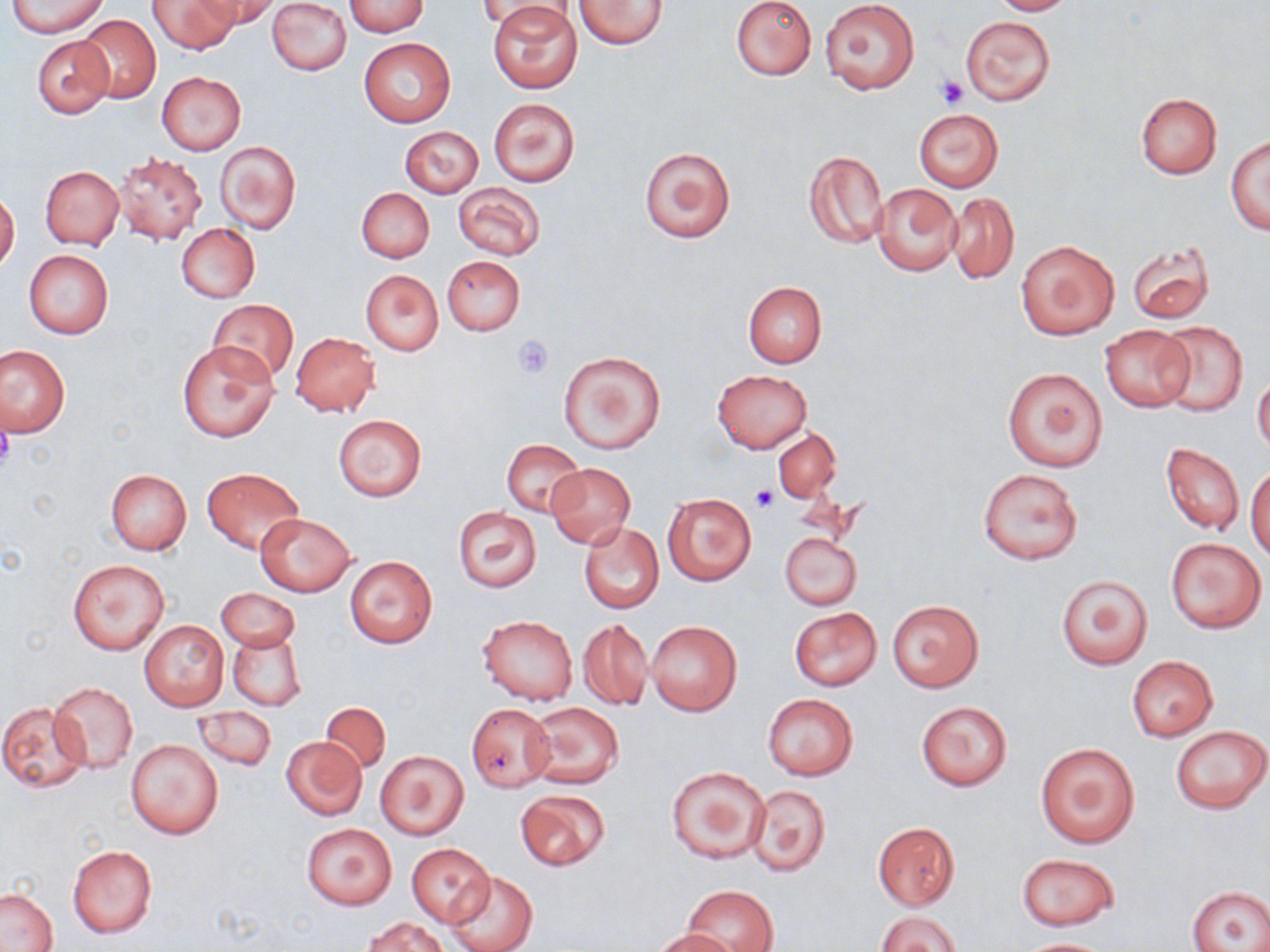

Approximate bounding boxes as named x1/y1/x2/y2 corners in pixels. Uninfected red blood cell locations: (x1=7, y1=0, x2=109, y2=38), (x1=148, y1=0, x2=237, y2=54), (x1=195, y1=0, x2=281, y2=34), (x1=267, y1=0, x2=352, y2=75), (x1=480, y1=0, x2=580, y2=28), (x1=731, y1=0, x2=817, y2=82), (x1=820, y1=0, x2=920, y2=93), (x1=991, y1=0, x2=1074, y2=15), (x1=343, y1=1, x2=429, y2=36), (x1=489, y1=1, x2=582, y2=94), (x1=574, y1=1, x2=668, y2=49), (x1=74, y1=14, x2=161, y2=103), (x1=961, y1=15, x2=1055, y2=106), (x1=33, y1=35, x2=115, y2=118), (x1=359, y1=38, x2=456, y2=128), (x1=157, y1=72, x2=247, y2=155), (x1=1134, y1=92, x2=1223, y2=180), (x1=489, y1=98, x2=579, y2=186), (x1=912, y1=108, x2=1004, y2=192), (x1=401, y1=126, x2=483, y2=197), (x1=1226, y1=136, x2=1270, y2=234), (x1=217, y1=142, x2=300, y2=234), (x1=638, y1=146, x2=736, y2=242), (x1=802, y1=148, x2=890, y2=250), (x1=113, y1=150, x2=206, y2=244), (x1=41, y1=165, x2=123, y2=249), (x1=871, y1=182, x2=962, y2=277), (x1=453, y1=183, x2=545, y2=259), (x1=356, y1=187, x2=434, y2=263), (x1=947, y1=192, x2=1019, y2=285), (x1=0, y1=193, x2=19, y2=271), (x1=177, y1=225, x2=259, y2=302), (x1=1016, y1=239, x2=1120, y2=340), (x1=1128, y1=244, x2=1214, y2=325), (x1=23, y1=249, x2=113, y2=339), (x1=442, y1=255, x2=525, y2=335), (x1=361, y1=269, x2=443, y2=355), (x1=742, y1=281, x2=827, y2=367), (x1=207, y1=300, x2=297, y2=383), (x1=1155, y1=322, x2=1247, y2=416), (x1=1101, y1=327, x2=1193, y2=412), (x1=290, y1=332, x2=381, y2=418), (x1=176, y1=341, x2=279, y2=443), (x1=1, y1=345, x2=69, y2=436), (x1=559, y1=350, x2=665, y2=454), (x1=1001, y1=365, x2=1108, y2=473), (x1=712, y1=370, x2=812, y2=452), (x1=1253, y1=371, x2=1270, y2=458), (x1=334, y1=414, x2=427, y2=500), (x1=774, y1=430, x2=841, y2=501), (x1=503, y1=440, x2=585, y2=517), (x1=1161, y1=442, x2=1244, y2=536), (x1=1246, y1=460, x2=1270, y2=561), (x1=546, y1=463, x2=635, y2=548), (x1=979, y1=467, x2=1082, y2=565), (x1=202, y1=468, x2=304, y2=554), (x1=105, y1=469, x2=192, y2=555), (x1=663, y1=494, x2=756, y2=584), (x1=452, y1=507, x2=541, y2=592), (x1=255, y1=513, x2=357, y2=596), (x1=579, y1=522, x2=664, y2=613), (x1=779, y1=532, x2=862, y2=610), (x1=1164, y1=536, x2=1266, y2=633), (x1=68, y1=557, x2=170, y2=656), (x1=345, y1=557, x2=437, y2=647), (x1=1054, y1=575, x2=1152, y2=670), (x1=217, y1=588, x2=299, y2=652), (x1=887, y1=600, x2=983, y2=693), (x1=788, y1=607, x2=883, y2=691), (x1=477, y1=616, x2=578, y2=705), (x1=577, y1=618, x2=652, y2=710), (x1=139, y1=619, x2=229, y2=711), (x1=646, y1=621, x2=742, y2=715), (x1=227, y1=631, x2=306, y2=710), (x1=1128, y1=656, x2=1216, y2=740), (x1=50, y1=682, x2=139, y2=773), (x1=763, y1=693, x2=859, y2=781), (x1=319, y1=700, x2=390, y2=773), (x1=1, y1=701, x2=91, y2=792), (x1=915, y1=701, x2=1012, y2=790), (x1=525, y1=702, x2=625, y2=789), (x1=465, y1=703, x2=554, y2=792), (x1=194, y1=707, x2=277, y2=770), (x1=1170, y1=724, x2=1268, y2=815), (x1=282, y1=735, x2=366, y2=820), (x1=127, y1=738, x2=224, y2=839), (x1=1034, y1=742, x2=1140, y2=848), (x1=376, y1=751, x2=468, y2=840), (x1=667, y1=766, x2=770, y2=864), (x1=746, y1=783, x2=832, y2=877), (x1=515, y1=790, x2=609, y2=870), (x1=873, y1=821, x2=961, y2=909), (x1=302, y1=822, x2=397, y2=911), (x1=405, y1=842, x2=495, y2=926), (x1=68, y1=845, x2=157, y2=937), (x1=1016, y1=853, x2=1119, y2=930), (x1=447, y1=870, x2=538, y2=952), (x1=684, y1=885, x2=777, y2=952), (x1=1187, y1=887, x2=1270, y2=951), (x1=1, y1=889, x2=57, y2=951), (x1=877, y1=911, x2=961, y2=952), (x1=366, y1=917, x2=449, y2=952), (x1=651, y1=928, x2=739, y2=952), (x1=1013, y1=938, x2=1119, y2=951). Platelet locations: (x1=935, y1=75, x2=969, y2=109), (x1=512, y1=335, x2=555, y2=377), (x1=0, y1=421, x2=14, y2=472), (x1=750, y1=486, x2=774, y2=511). Slide-level diagnosis: negative for blood parasites. Single field of view. Image is 1270×952 pixels. Captured at 1000x magnification. Light microscopy. May-Grünwald-Giemsa stain. Thin blood smear.